Outline each blood parasite and name the species.
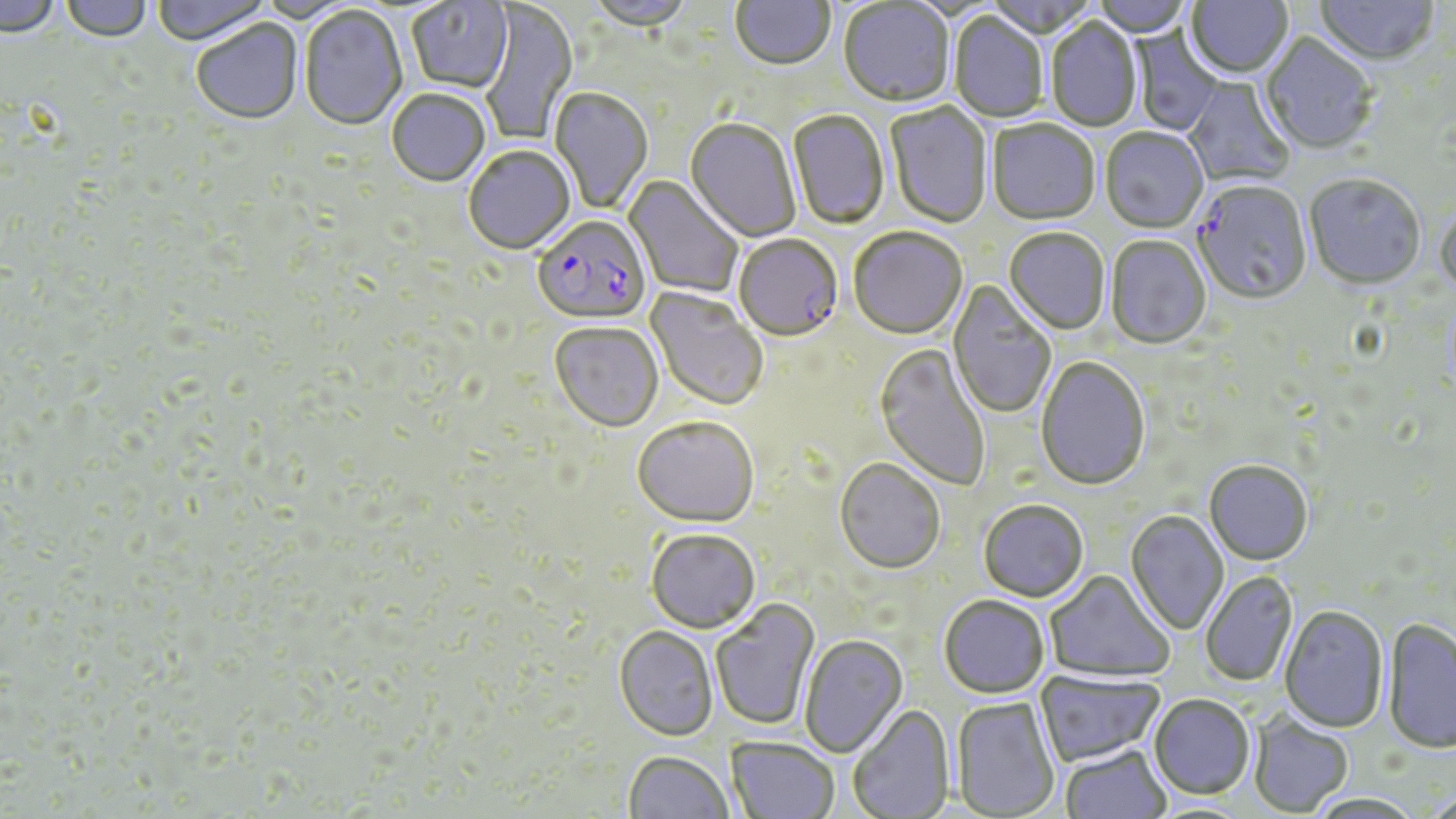
Approximate bounding boxes as named x1/y1/x2/y2 corners in pixels.
Plasmodium falciparum-infected red blood cells: (x1=1192, y1=181, x2=1313, y2=308), (x1=533, y1=216, x2=653, y2=329), (x1=734, y1=236, x2=843, y2=344).
No Plasmodium ovale, Plasmodium malariae, Plasmodium vivax, Babesia divergens, or Trypanosoma brucei observed.

Summary:
  - Uninfected red blood cell locations: (x1=0, y1=0, x2=61, y2=40), (x1=60, y1=0, x2=153, y2=45), (x1=151, y1=0, x2=272, y2=48), (x1=730, y1=0, x2=836, y2=74), (x1=984, y1=0, x2=1097, y2=41), (x1=1092, y1=0, x2=1192, y2=39), (x1=1186, y1=0, x2=1293, y2=81), (x1=1316, y1=0, x2=1438, y2=68), (x1=406, y1=1, x2=513, y2=95), (x1=586, y1=1, x2=695, y2=33), (x1=480, y1=2, x2=578, y2=146), (x1=839, y1=2, x2=955, y2=109), (x1=299, y1=7, x2=407, y2=133), (x1=948, y1=12, x2=1048, y2=124), (x1=1045, y1=17, x2=1143, y2=134), (x1=191, y1=21, x2=303, y2=127), (x1=1130, y1=27, x2=1223, y2=136), (x1=1259, y1=34, x2=1377, y2=157), (x1=1184, y1=76, x2=1296, y2=188), (x1=549, y1=88, x2=653, y2=215), (x1=386, y1=90, x2=490, y2=189), (x1=885, y1=102, x2=993, y2=230), (x1=787, y1=110, x2=889, y2=231), (x1=684, y1=119, x2=801, y2=243), (x1=987, y1=120, x2=1100, y2=227), (x1=1100, y1=129, x2=1208, y2=235), (x1=463, y1=148, x2=575, y2=256), (x1=624, y1=175, x2=743, y2=298), (x1=1304, y1=176, x2=1426, y2=293), (x1=1435, y1=206, x2=1456, y2=302), (x1=848, y1=229, x2=968, y2=342), (x1=1004, y1=229, x2=1110, y2=336), (x1=1106, y1=236, x2=1211, y2=350), (x1=948, y1=279, x2=1056, y2=420), (x1=645, y1=287, x2=768, y2=413), (x1=550, y1=324, x2=663, y2=434), (x1=875, y1=343, x2=991, y2=492), (x1=1036, y1=356, x2=1151, y2=492), (x1=632, y1=418, x2=759, y2=528), (x1=835, y1=459, x2=945, y2=575), (x1=1204, y1=461, x2=1313, y2=565), (x1=979, y1=501, x2=1088, y2=603), (x1=1125, y1=511, x2=1229, y2=635), (x1=646, y1=528, x2=760, y2=633), (x1=1045, y1=570, x2=1175, y2=683), (x1=1200, y1=571, x2=1298, y2=686), (x1=938, y1=596, x2=1049, y2=700), (x1=711, y1=599, x2=820, y2=731), (x1=1279, y1=606, x2=1389, y2=734), (x1=1383, y1=618, x2=1456, y2=755), (x1=614, y1=626, x2=718, y2=740), (x1=799, y1=634, x2=908, y2=758), (x1=1035, y1=669, x2=1164, y2=766), (x1=1148, y1=694, x2=1255, y2=800), (x1=951, y1=697, x2=1060, y2=818), (x1=847, y1=705, x2=954, y2=819), (x1=1248, y1=713, x2=1353, y2=816), (x1=726, y1=736, x2=839, y2=819), (x1=1061, y1=744, x2=1172, y2=819), (x1=623, y1=751, x2=734, y2=819), (x1=1420, y1=790, x2=1456, y2=819), (x1=1304, y1=794, x2=1425, y2=819)
  - Slide-level diagnosis: Plasmodium falciparum
  - Field of view: one of a larger specimen
  - Magnification: 1000x
  - Modality: light microscopy
  - Preparation: thin blood smear
  - Stain: May-Grünwald-Giemsa
  - Image size: 1456×819 pixels